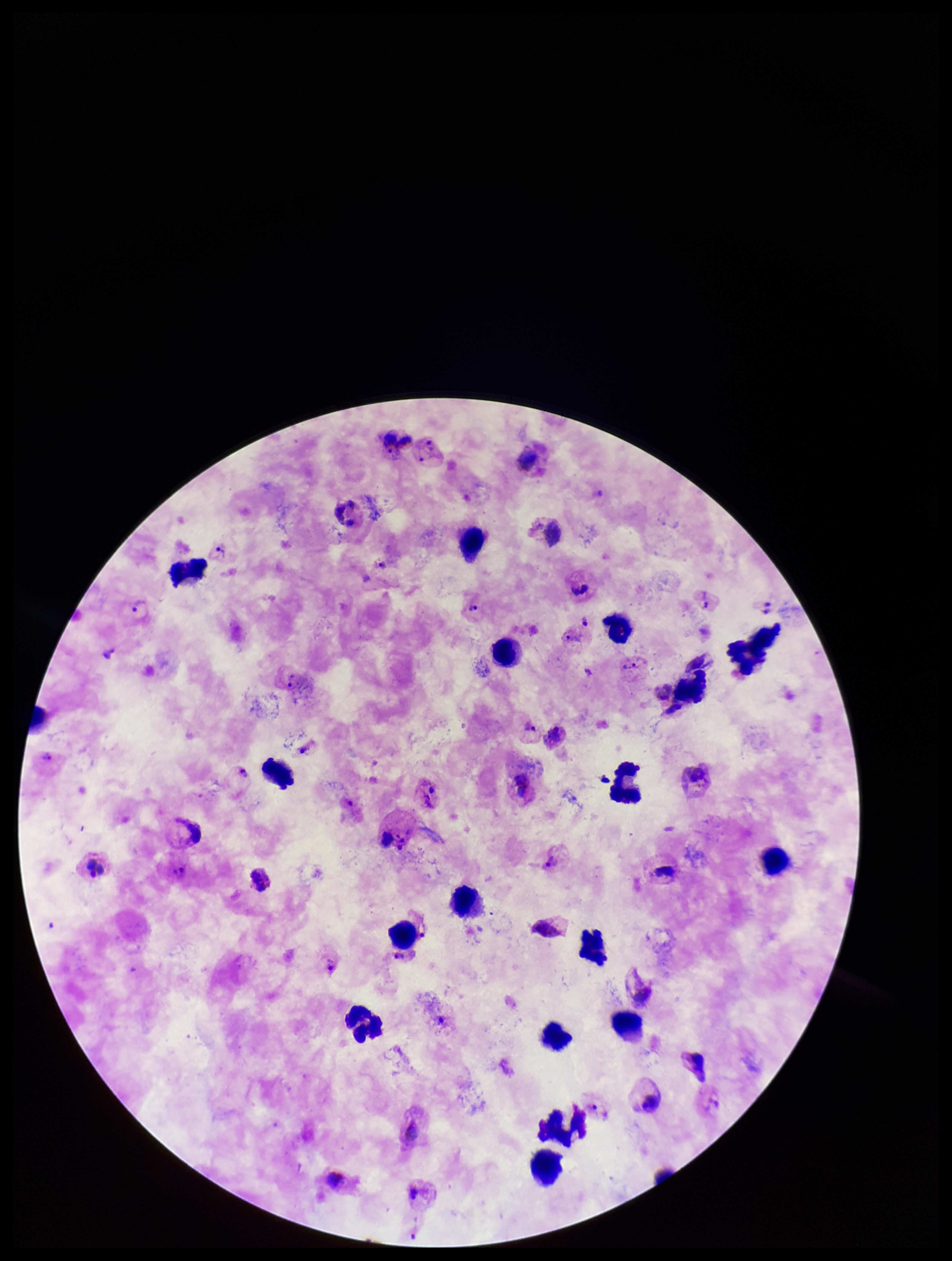
Summary:
  - Plasmodium parasites: seen
  - Parasite count: 8
  - Field of view: single
  - Image size: 952×1261 pixels
  - Leukocyte count: 21
  - Capture: smartphone photograph through the microscope eyepiece
  - Preparation: thick blood smear
  - Patient malaria status: infected
  - Stain: Giemsa
  - Species reported for this patient: Plasmodium vivax